Assess this cell for malaria.
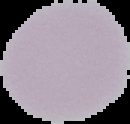
It is uninfected.

The area outside the segmented cell region is set to black. Image is 130×124 pixels. From a thin blood film.